Identify the parasite.
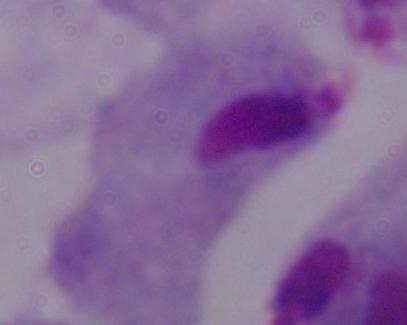

This is a trichomonad.

Summary:
  - Magnification: 1000x
  - Modality: photomicrograph